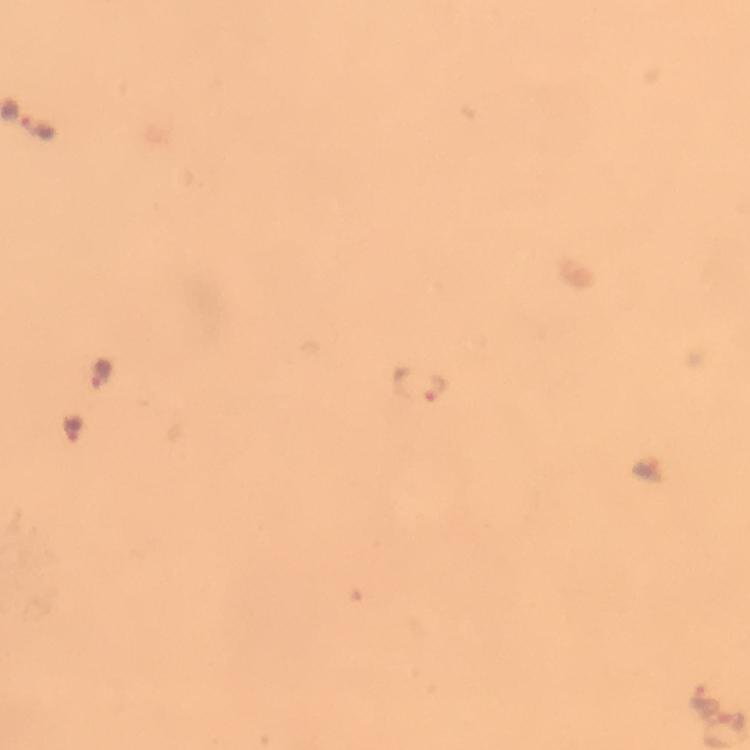

{
  "immersion_oil": "applied",
  "image_size": "750×750 pixels",
  "capture": "smartphone mounted on the microscope",
  "cropped_from": "one field of view",
  "malaria_parasite_locations": "approximate centers as [x, y] in pixels: [421, 383], [706, 698]",
  "stain": "Giemsa",
  "magnification": "100x",
  "context": "from a malaria diagnostic workup",
  "preparation": "thick blood smear"
}